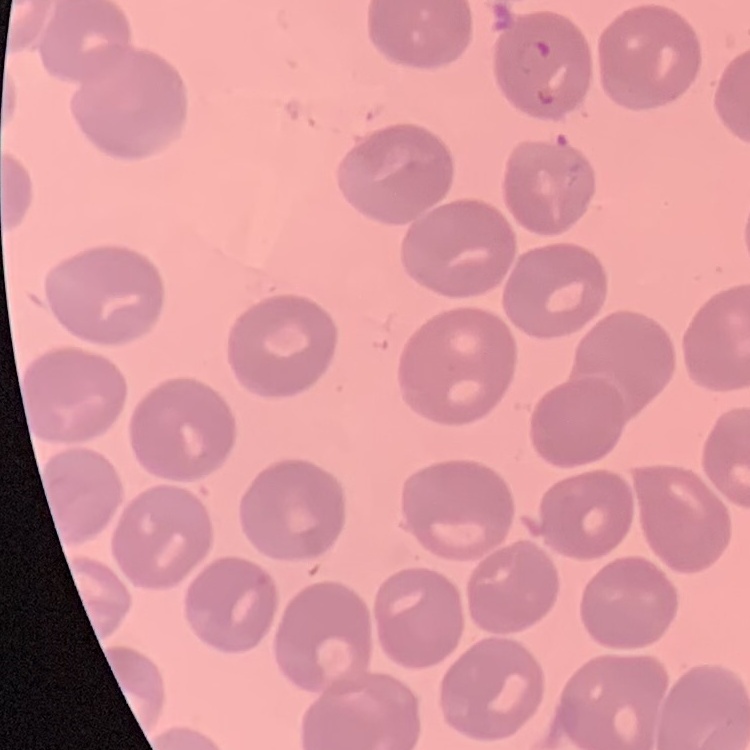

red blood cell morphology = no rouleaux formation
image type = square crop of a larger photomicrograph
stain = Field's or Giemsa
preparation = thin blood smear